Locate every Trypanosoma brucei.
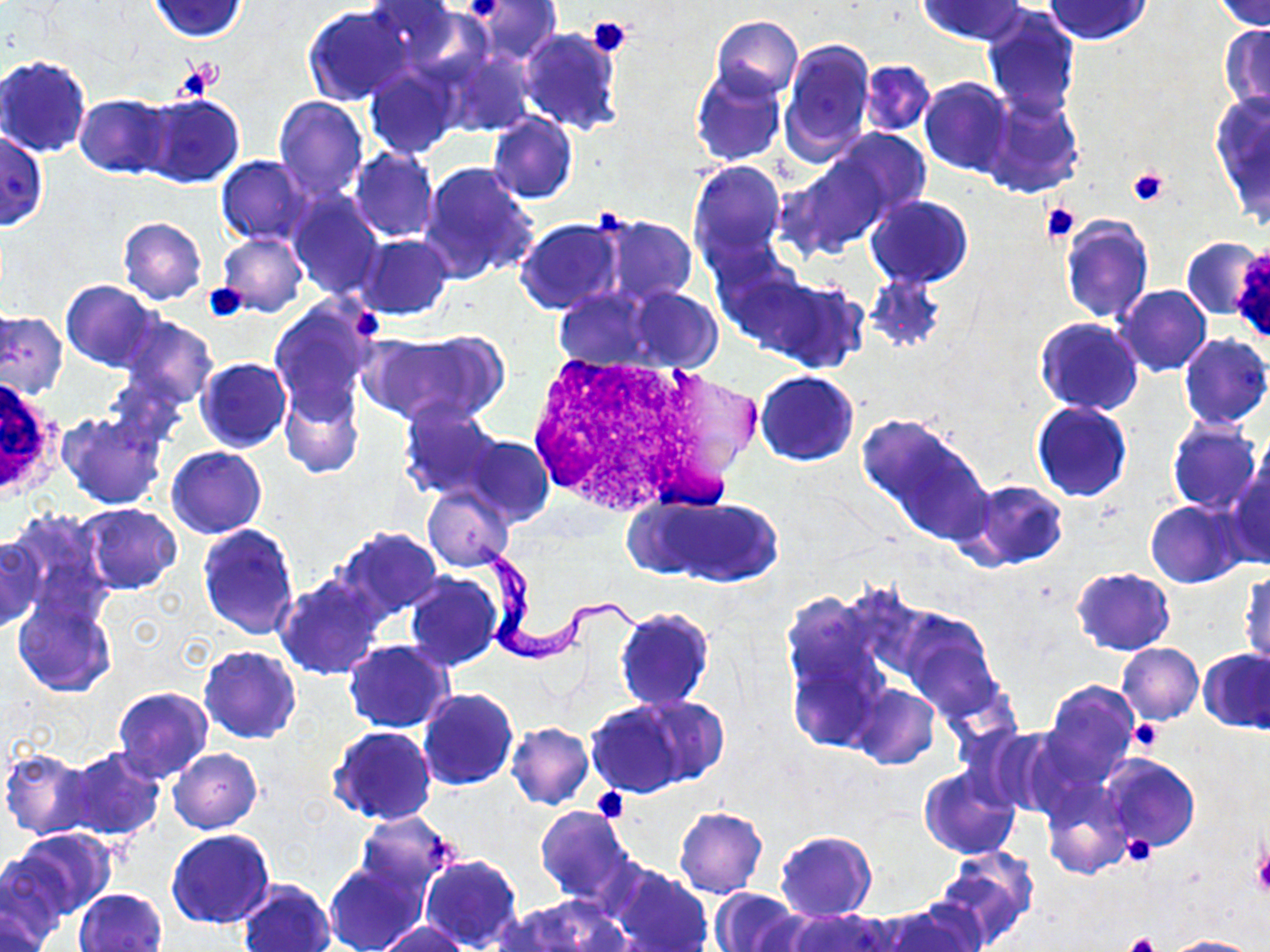

Approximate bounding boxes as [x1, y1, x2, y2] in pixels.
Trypanosoma brucei: [467, 536, 662, 663].

White blood cell locations: [531, 347, 728, 515], [0, 372, 63, 506]. Platelet locations: [461, 0, 508, 23], [588, 16, 632, 57], [181, 66, 212, 100], [1128, 165, 1170, 207], [1041, 201, 1079, 242], [598, 204, 627, 236], [201, 283, 248, 322], [1129, 718, 1163, 752], [591, 787, 629, 824], [1122, 835, 1155, 866], [1251, 850, 1270, 898], [1124, 932, 1158, 952]. Uninfected red blood cell locations: [149, 0, 249, 41], [362, 0, 462, 62], [471, 0, 560, 62], [919, 0, 1026, 44], [1044, 0, 1152, 44], [1214, 1, 1270, 31], [303, 5, 411, 106], [981, 7, 1080, 120], [710, 16, 803, 102], [1220, 24, 1270, 112], [518, 27, 622, 136], [779, 37, 876, 163], [439, 46, 533, 138], [0, 55, 92, 157], [859, 60, 935, 137], [364, 65, 461, 159], [690, 67, 786, 166], [919, 77, 1014, 176], [983, 92, 1085, 198], [136, 93, 244, 189], [1210, 93, 1270, 228], [75, 94, 172, 177], [274, 96, 368, 200], [487, 112, 577, 203], [831, 128, 931, 218], [0, 129, 48, 231], [349, 148, 438, 241], [216, 155, 314, 245], [786, 155, 890, 257], [688, 159, 787, 270], [418, 163, 539, 283], [289, 190, 385, 300], [866, 195, 973, 288], [592, 214, 697, 307], [1060, 214, 1153, 326], [118, 217, 207, 304], [514, 218, 621, 315], [218, 233, 308, 317], [356, 234, 453, 320], [1182, 237, 1268, 320], [750, 274, 867, 374], [866, 276, 945, 353], [62, 280, 161, 371], [1115, 285, 1211, 376], [627, 287, 720, 371], [554, 288, 655, 372], [268, 299, 378, 419], [0, 311, 67, 400], [119, 315, 218, 410], [1034, 318, 1144, 416], [1178, 334, 1270, 430], [356, 335, 495, 425], [196, 357, 291, 452], [754, 370, 859, 466], [279, 382, 364, 480], [398, 402, 506, 503], [1032, 402, 1132, 502], [58, 410, 167, 511], [860, 415, 992, 544], [1168, 419, 1261, 515], [464, 435, 553, 528], [167, 446, 267, 538], [1225, 458, 1270, 569], [963, 479, 1069, 571], [424, 485, 514, 573], [650, 496, 784, 587], [1145, 500, 1247, 587], [78, 503, 183, 595], [4, 509, 116, 631], [198, 524, 299, 638], [334, 527, 445, 621], [0, 533, 44, 633], [1240, 566, 1269, 669], [1071, 568, 1174, 655], [404, 573, 503, 672], [274, 574, 385, 680], [783, 593, 893, 753], [11, 596, 117, 697], [614, 606, 713, 711], [899, 609, 1001, 720], [344, 640, 453, 732], [1117, 643, 1203, 723], [199, 645, 300, 743], [1200, 648, 1269, 732], [1041, 679, 1140, 783], [851, 684, 939, 769], [113, 686, 214, 782], [417, 687, 518, 790], [621, 694, 731, 788], [583, 701, 693, 798], [506, 722, 593, 810], [328, 725, 437, 825], [62, 746, 165, 840], [168, 747, 262, 833], [0, 748, 96, 840], [1100, 754, 1199, 852], [918, 765, 1020, 859], [1040, 783, 1131, 881], [534, 806, 639, 906], [674, 807, 767, 898], [354, 812, 457, 900], [12, 828, 118, 917], [166, 829, 275, 929], [775, 830, 877, 922], [0, 849, 75, 945], [932, 849, 1040, 949], [419, 854, 522, 950], [324, 860, 426, 952], [607, 865, 712, 952], [239, 878, 335, 952], [74, 888, 167, 952], [710, 888, 803, 952], [1, 896, 54, 952], [497, 898, 622, 952], [876, 902, 985, 952], [781, 910, 894, 952], [377, 920, 471, 952], [1164, 935, 1261, 952]. Slide-level diagnosis: Trypanosoma brucei. One field of a larger specimen. 1000x magnification. Image is 1270×952 pixels. Light microscopy. Thin blood film. May-Grünwald-Giemsa-stained preparation.